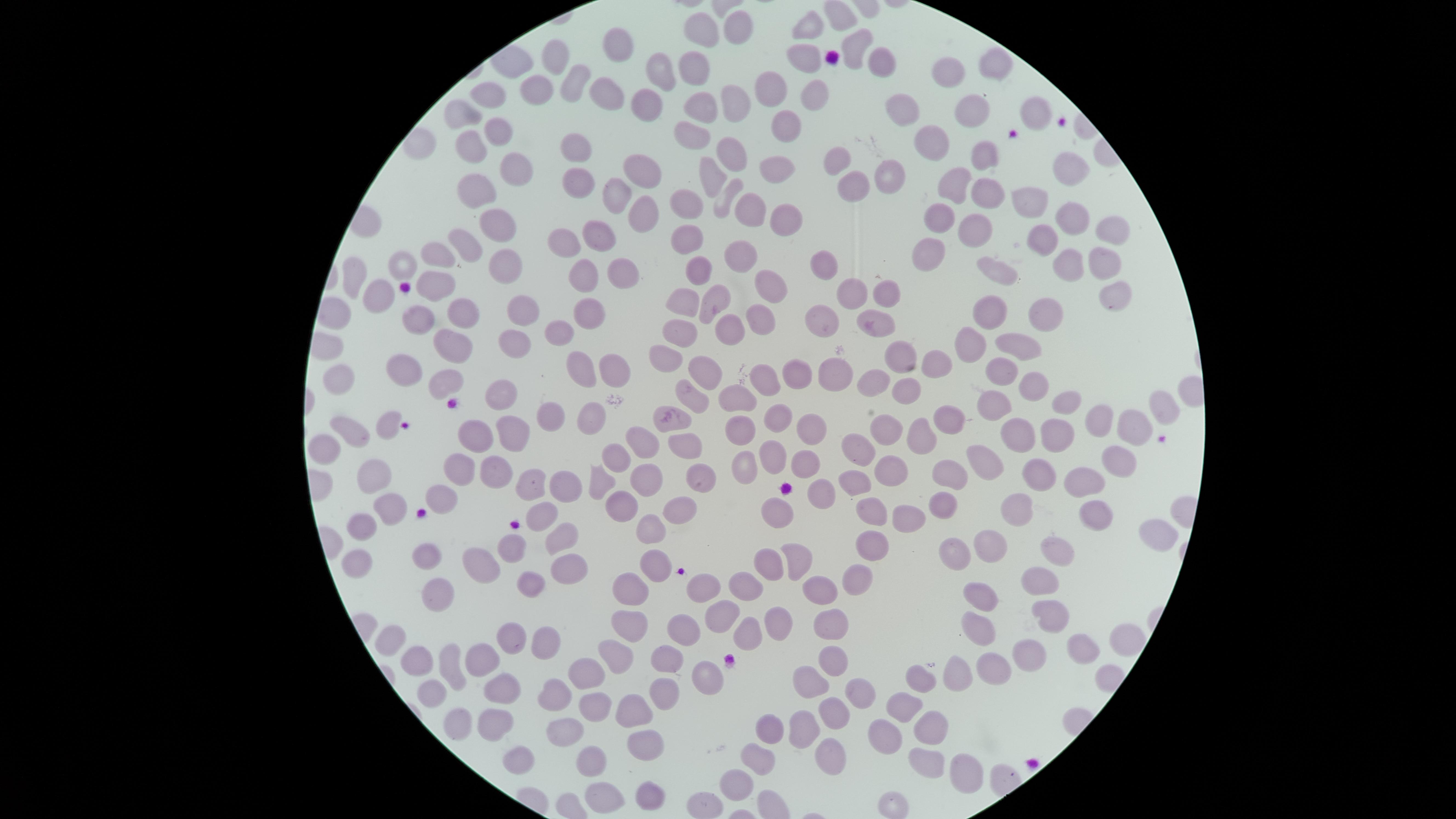 Approximate marker points as (x, y) in pixels. Uninfected red blood cells: (809, 29), (739, 31), (705, 34), (618, 41), (853, 44), (558, 59), (805, 59), (879, 60), (995, 62), (945, 69), (697, 73), (664, 75), (577, 82), (537, 85), (603, 89), (771, 90), (815, 90), (497, 97), (730, 101), (647, 106), (701, 106), (1034, 108), (898, 110), (966, 112), (468, 113), (784, 120), (497, 125), (688, 131), (936, 137), (468, 143), (419, 144), (572, 146), (733, 148), (983, 152), (838, 160), (637, 165), (514, 167), (1064, 169), (780, 171), (890, 172), (711, 176), (577, 179), (853, 181), (952, 181), (479, 185), (620, 190), (991, 190), (722, 193), (1029, 199), (685, 205), (746, 206), (639, 214), (939, 214), (787, 217), (1071, 218), (498, 224), (972, 227), (1111, 227), (692, 237), (1043, 237), (597, 242), (562, 245), (466, 248), (926, 248), (440, 252), (746, 258), (1101, 260), (503, 261), (822, 262), (1069, 264), (404, 267), (620, 269), (1001, 269), (582, 273), (698, 273), (436, 280), (360, 281), (779, 283), (850, 291), (1113, 293), (378, 295), (884, 295), (683, 301), (714, 302), (587, 310), (522, 312), (985, 312), (464, 313), (417, 316), (1043, 316), (874, 321), (762, 324), (830, 325), (562, 327), (730, 328), (682, 333), (967, 341), (1016, 341), (515, 343), (452, 346), (905, 350), (665, 357), (934, 361), (609, 365), (703, 366), (576, 370), (995, 370), (407, 372), (832, 372), (344, 376), (803, 376), (447, 377), (768, 381), (870, 383), (907, 385), (1034, 385), (693, 394), (733, 394), (499, 395), (1069, 402), (995, 404), (1166, 407), (593, 413), (776, 414), (1095, 414), (549, 415), (950, 417), (672, 420), (884, 420), (386, 422), (737, 422), (809, 422), (1129, 423), (351, 424), (476, 429), (508, 431), (1056, 431), (923, 433), (1020, 434), (686, 439), (642, 440), (856, 446), (323, 447), (775, 452), (619, 458), (979, 460), (1119, 462), (805, 465), (745, 466), (460, 468), (893, 469), (491, 472), (1043, 472), (373, 475), (697, 476), (954, 477), (647, 478), (1085, 480), (601, 481), (534, 483), (857, 484), (570, 485), (822, 493), (439, 497), (387, 501), (943, 504), (622, 506), (1022, 507), (677, 508), (776, 510), (543, 512), (870, 514), (1092, 517), (914, 521), (654, 525), (365, 531), (1150, 533), (563, 536), (989, 541), (512, 544), (870, 545), (949, 548), (1055, 548), (426, 555), (798, 555), (355, 558), (651, 564), (567, 566), (765, 567), (481, 570), (857, 575), (527, 580), (1041, 583), (824, 585), (745, 587), (706, 588), (435, 589), (631, 590), (980, 595), (721, 615), (772, 618), (1050, 618), (830, 624), (629, 629), (686, 630), (987, 632), (743, 633), (510, 636), (1125, 639), (395, 640), (544, 643), (1084, 648), (1025, 654), (669, 656), (614, 657), (483, 658), (988, 659), (829, 661), (423, 663), (452, 664), (955, 673), (588, 676), (701, 680), (922, 680), (814, 682), (858, 692), (504, 693), (665, 693), (432, 694), (552, 697), (902, 705), (591, 707), (839, 708), (639, 709), (485, 722), (450, 726), (772, 728), (931, 728), (805, 729), (562, 731), (886, 733), (646, 743), (833, 755), (757, 757), (518, 759), (926, 760), (589, 763), (964, 767), (742, 779), (651, 796), (605, 798), (895, 799), (701, 805). Presence: no malaria parasites identified. Photographed with a smartphone camera through the microscope eyepiece. Thin smear of blood. Circular visible region. Image is 1456×819 pixels. Single field of view. Giemsa-stained preparation.